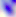

Micrograph. 400x magnification. Toxoplasma gondii is shown.